Give the position of every leukocyte visible.
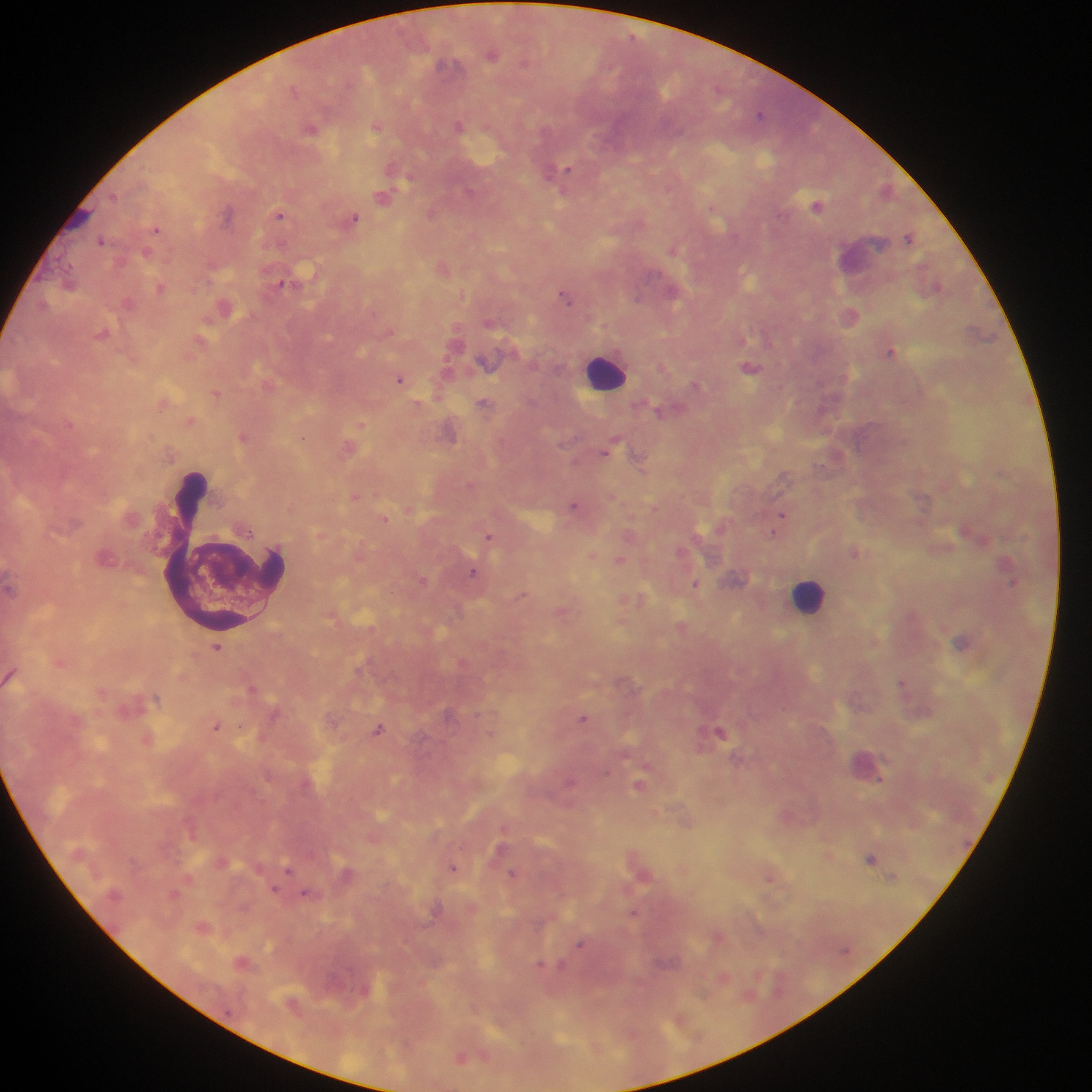
Approximate centers as x y in pixels.
Leukocytes: 605 372; 222 555; 809 596.

preparation = thick blood smear
country = Ghana
image size = 1092×1092 pixels
field of view = single
malaria parasite locations = approximate centers as x y in pixels: 492 53; 524 63; 446 65; 293 89; 760 113; 376 126; 458 126; 311 128; 393 169; 565 170; 469 192; 115 197; 382 197; 817 205; 227 213; 430 213; 280 215; 354 219; 156 229; 908 237; 102 240; 672 249; 147 253; 281 283; 160 288; 673 293; 638 297; 565 298; 102 333; 891 352; 750 367; 400 379; 695 383; 216 393; 484 402; 659 411; 361 425; 244 437; 303 437; 607 449; 638 459; 356 497; 573 505; 782 515; 385 518; 250 533; 774 534; 489 537; 855 552; 592 555; 619 560; 473 572; 422 581; 1012 583; 695 585; 522 595; 961 642; 217 649; 902 682; 156 698; 448 714; 582 718; 216 727; 378 729; 720 731; 639 785; 871 859; 452 868; 289 869; 513 873; 892 877; 770 878; 275 890; 306 894; 634 913; 579 944; 540 965; 461 1058
capture = mobile-phone photograph through a microscope